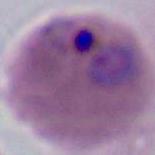

Summary:
  - Modality: photomicrograph
  - Magnification: 400x or 1000x
  - Identification: Plasmodium